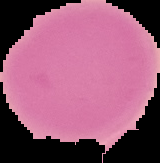

image size = 160×163 pixels
result = no malaria parasites seen
preparation = thin blood smear
image type = cell region segmented out of the field of view; surrounding area masked to black